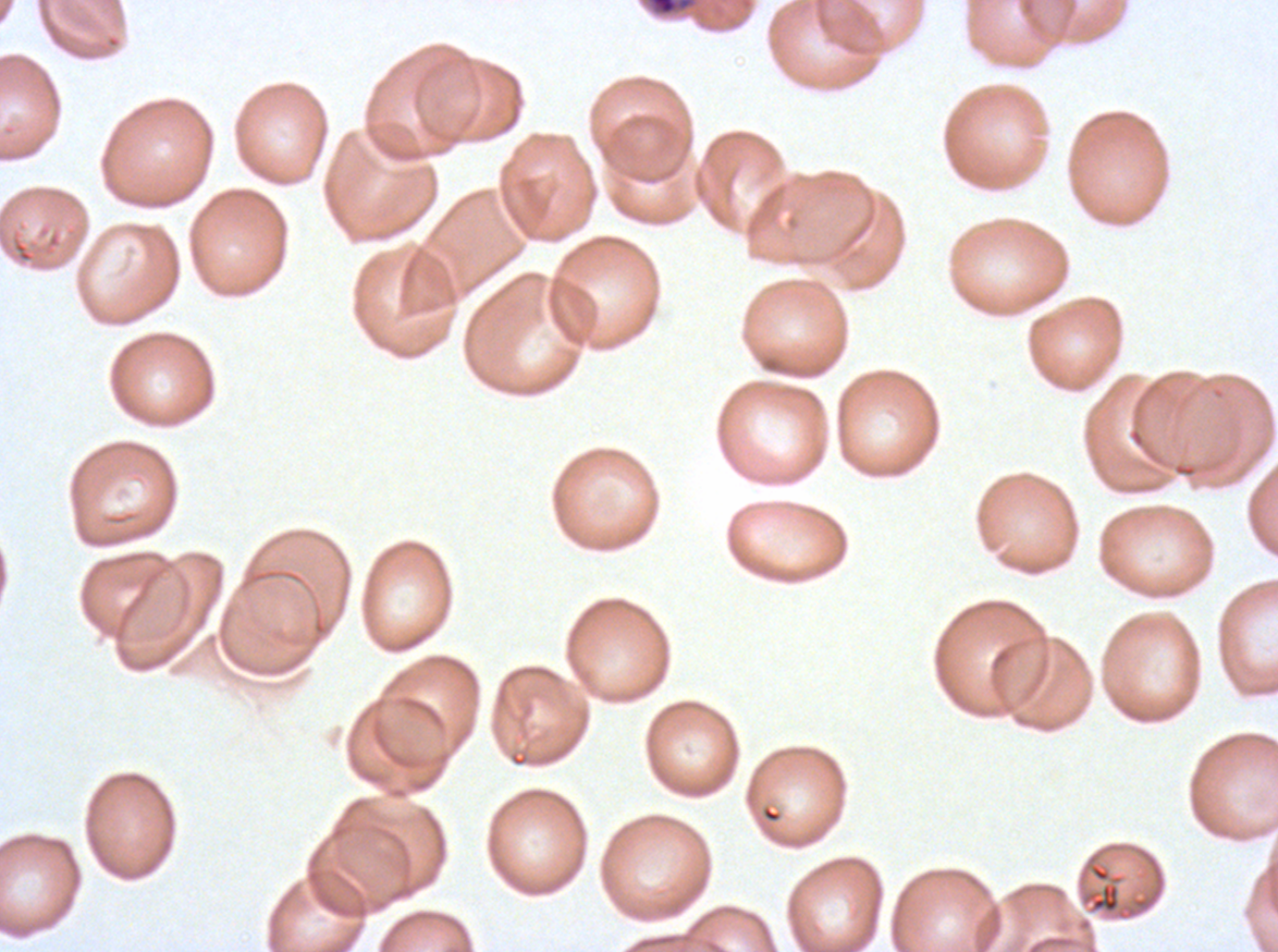

notation = approximate bounding boxes as (x1, y1, x2, y2) in pixels
debris locations = (644, 0, 699, 18), (1081, 854, 1162, 921)
image size = 1278×952 pixels
field of view = one sub-image of a larger composite
specimen = ex-vivo Plasmodium falciparum culture from a patient in The Gambia, grown for 24 to 48 hours
stain = Giemsa
preparation = thin blood film